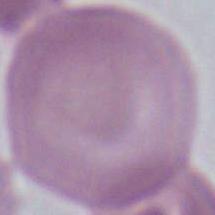
Summary:
  - Magnification: 1000x
  - Modality: photomicrograph
  - Identification: red blood cell